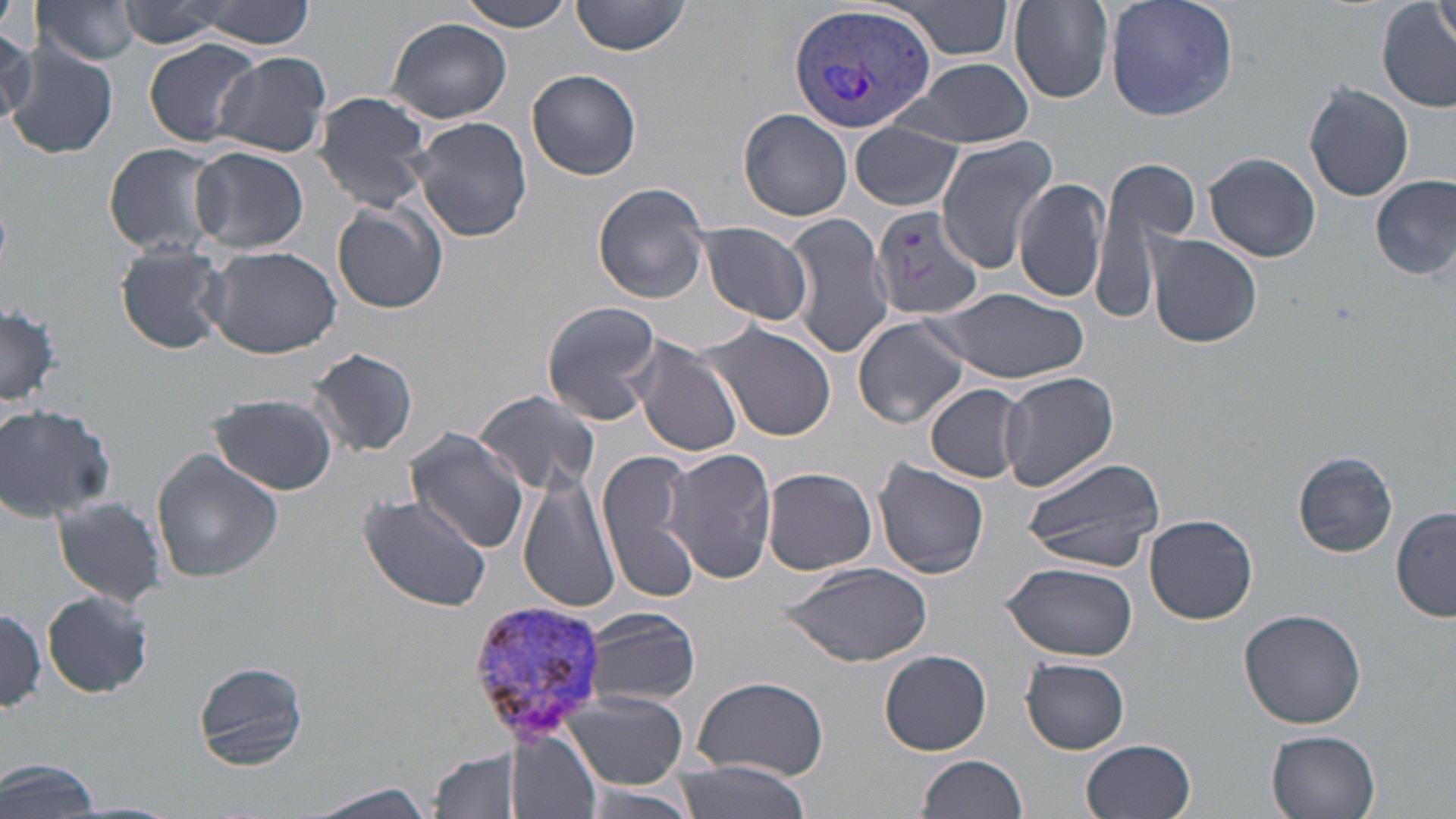

slide-level diagnosis = Plasmodium vivax
preparation = thin blood film
uninfected red blood cell locations = approximate bounding boxes as [x1, y1, x2, y2] in pixels: [464, 0, 575, 31], [570, 0, 690, 57], [894, 0, 1015, 58], [1005, 0, 1116, 104], [1103, 0, 1239, 121], [1434, 0, 1456, 53], [36, 1, 143, 66], [118, 1, 227, 47], [191, 1, 316, 49], [1379, 3, 1455, 112], [387, 17, 512, 123], [0, 28, 40, 122], [144, 39, 260, 147], [5, 45, 118, 159], [214, 51, 332, 158], [901, 57, 1033, 148], [527, 69, 642, 182], [1304, 82, 1415, 201], [313, 91, 434, 209], [740, 109, 852, 221], [412, 115, 532, 244], [850, 121, 964, 211], [936, 136, 1058, 270], [102, 143, 227, 257], [191, 146, 309, 253], [1204, 152, 1320, 262], [1105, 157, 1200, 245], [1015, 176, 1110, 304], [1373, 176, 1454, 280], [593, 180, 712, 304], [332, 202, 448, 315], [784, 211, 896, 359], [696, 221, 815, 327], [1145, 234, 1263, 349], [116, 241, 228, 353], [201, 244, 343, 357], [933, 288, 1088, 385], [541, 301, 664, 427], [1, 303, 64, 409], [850, 315, 971, 429], [703, 320, 840, 443], [629, 338, 745, 458], [309, 346, 418, 458], [999, 371, 1119, 492], [926, 384, 1027, 485], [474, 390, 601, 494], [210, 394, 337, 496], [0, 404, 119, 522], [407, 431, 528, 551], [152, 448, 283, 583], [663, 448, 776, 583], [600, 449, 701, 603], [1295, 452, 1396, 557], [1021, 457, 1165, 572], [874, 460, 990, 579], [762, 467, 877, 574], [519, 470, 623, 612], [357, 492, 494, 612], [50, 500, 170, 609], [1392, 506, 1455, 624], [1145, 512, 1258, 623], [1003, 561, 1137, 661], [778, 562, 932, 667], [42, 590, 152, 700], [0, 604, 46, 713], [582, 607, 699, 707], [1238, 609, 1368, 730], [880, 650, 992, 753], [1022, 658, 1129, 753], [194, 659, 311, 771], [692, 675, 828, 781], [566, 692, 690, 789], [1266, 729, 1381, 818], [507, 733, 601, 818], [1081, 739, 1196, 819], [427, 746, 527, 819], [918, 755, 1027, 819], [0, 757, 103, 819], [670, 761, 813, 819], [575, 783, 700, 819], [285, 784, 450, 819]
image size = 1456×819 pixels
magnification = 1000x
field of view = one of a larger specimen
stain = May-Grünwald-Giemsa
Plasmodium vivax-infected red blood cell locations = approximate bounding boxes as [x1, y1, x2, y2] in pixels: [788, 2, 939, 138], [871, 206, 987, 319], [463, 599, 611, 746]
modality = light microscopy